Classify this cell by malaria status.
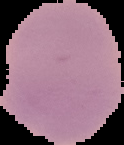
Uninfected.

{
  "image_type": "segmented cell region on a black background",
  "image_size": "124×145 pixels",
  "preparation": "thin blood film"
}